Locate and identify every blood parasite.
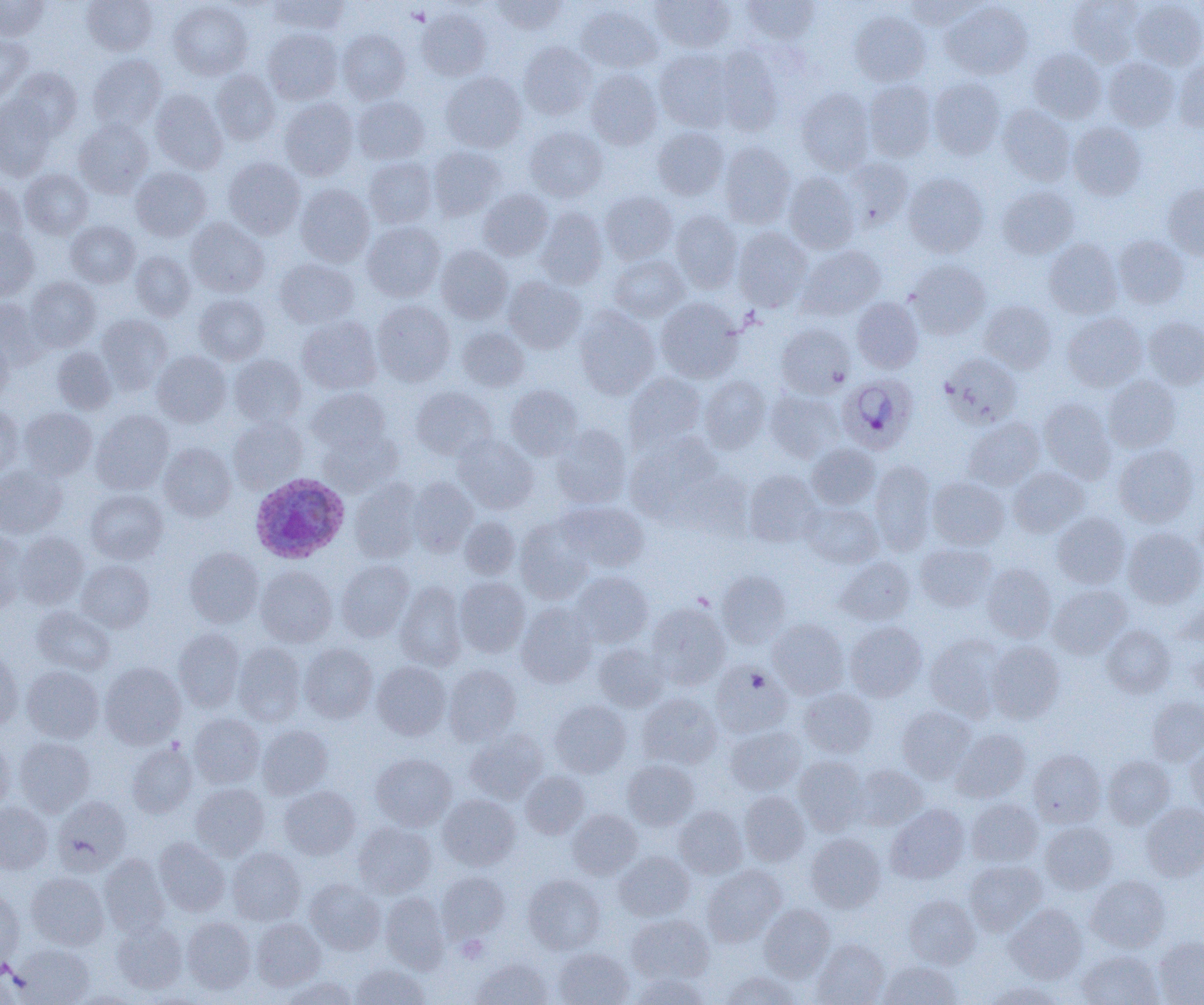

Approximate bounding boxes as [x1, y1, x2, y2] in pixels.
Plasmodium ovale-infected red blood cells: [837, 375, 918, 454], [249, 473, 350, 563].
No Plasmodium falciparum, Plasmodium malariae, Plasmodium vivax, Babesia divergens, or Trypanosoma brucei observed.

Summary:
  - Uninfected red blood cell locations: [82, 0, 157, 55], [268, 0, 350, 34], [489, 0, 567, 34], [651, 0, 736, 52], [740, 0, 820, 45], [903, 0, 982, 29], [1067, 0, 1143, 67], [0, 1, 49, 40], [168, 1, 252, 80], [942, 1, 1033, 79], [1130, 1, 1204, 70], [576, 4, 663, 73], [417, 7, 491, 81], [849, 10, 930, 86], [263, 28, 342, 104], [337, 29, 410, 103], [0, 34, 32, 102], [519, 42, 595, 120], [713, 45, 783, 135], [654, 49, 736, 132], [1028, 49, 1106, 122], [88, 54, 166, 132], [1103, 57, 1180, 131], [1174, 59, 1204, 132], [10, 68, 82, 138], [585, 68, 662, 150], [212, 70, 279, 145], [441, 72, 527, 152], [928, 77, 1005, 159], [864, 79, 937, 162], [150, 88, 227, 173], [796, 88, 875, 174], [0, 96, 56, 180], [352, 96, 430, 164], [280, 98, 358, 180], [998, 104, 1075, 185], [74, 119, 153, 198], [1069, 122, 1146, 200], [524, 126, 607, 202], [653, 127, 728, 200], [719, 142, 796, 228], [428, 146, 505, 220], [842, 156, 914, 231], [223, 157, 305, 239], [364, 157, 437, 228], [131, 166, 211, 241], [20, 169, 93, 238], [904, 172, 988, 257], [783, 173, 860, 253], [0, 181, 26, 249], [1163, 183, 1204, 260], [295, 184, 375, 266], [997, 186, 1079, 259], [478, 189, 553, 261], [600, 191, 677, 264], [535, 206, 608, 289], [670, 210, 743, 293], [186, 218, 269, 297], [66, 221, 139, 287], [363, 221, 445, 301], [733, 227, 812, 311], [0, 229, 38, 299], [1113, 234, 1190, 308], [1043, 239, 1122, 319], [436, 246, 513, 323], [798, 246, 886, 319], [130, 251, 196, 320], [608, 254, 689, 321], [275, 258, 358, 328], [907, 259, 991, 339], [25, 277, 101, 351], [503, 277, 586, 353], [194, 294, 270, 365], [851, 297, 923, 373], [655, 298, 744, 383], [0, 299, 46, 368], [372, 300, 455, 385], [980, 300, 1057, 372], [574, 307, 660, 399], [1062, 312, 1147, 391], [96, 314, 172, 393], [297, 315, 381, 394], [1142, 317, 1204, 389], [776, 323, 855, 398], [456, 327, 529, 392], [0, 336, 13, 403], [52, 347, 116, 415], [152, 350, 231, 427], [941, 353, 1022, 428], [229, 354, 306, 427], [625, 373, 707, 451], [700, 375, 772, 453], [1102, 376, 1181, 453], [506, 385, 584, 459], [411, 386, 496, 460], [307, 388, 389, 454], [765, 389, 845, 463], [1039, 398, 1117, 482], [0, 406, 23, 478], [19, 408, 97, 479], [92, 410, 174, 493], [229, 417, 307, 491], [963, 418, 1044, 490], [551, 425, 632, 508], [318, 429, 401, 496], [626, 433, 723, 520], [453, 434, 538, 514], [158, 443, 236, 521], [807, 443, 880, 510], [1113, 444, 1198, 526], [870, 460, 936, 554], [0, 464, 67, 538], [1008, 467, 1089, 537], [678, 469, 755, 540], [744, 469, 822, 547], [408, 477, 478, 556], [928, 477, 1009, 550], [348, 480, 423, 562], [86, 489, 168, 564], [559, 501, 650, 572], [801, 503, 883, 568], [1052, 512, 1130, 589], [460, 517, 520, 579], [515, 517, 594, 603], [1122, 527, 1204, 608], [0, 530, 27, 612], [14, 531, 89, 609], [915, 542, 997, 612], [184, 547, 264, 627], [836, 556, 916, 626], [77, 559, 154, 632], [336, 560, 414, 641], [982, 563, 1056, 642], [255, 566, 337, 647], [572, 571, 653, 648], [717, 571, 791, 648], [454, 577, 530, 657], [395, 581, 467, 670], [1048, 585, 1132, 658], [1175, 599, 1204, 646], [516, 602, 598, 687], [647, 602, 731, 689], [32, 606, 115, 675], [768, 618, 848, 699], [844, 621, 926, 702], [1102, 625, 1175, 697], [174, 629, 245, 711], [924, 634, 1006, 721], [987, 640, 1064, 723], [233, 643, 306, 725], [593, 643, 669, 711], [299, 644, 378, 722], [1187, 645, 1204, 701], [0, 650, 22, 731], [373, 661, 451, 741], [710, 661, 793, 739], [100, 662, 185, 748], [443, 665, 521, 744], [22, 666, 103, 743], [798, 688, 878, 757], [637, 692, 722, 769], [1147, 697, 1204, 765], [549, 699, 631, 777], [897, 705, 976, 783], [189, 713, 264, 788], [257, 725, 333, 799], [726, 726, 806, 795], [465, 729, 547, 804], [951, 729, 1031, 803], [14, 737, 95, 815], [0, 739, 14, 812], [126, 742, 197, 817], [1185, 742, 1204, 814], [1028, 749, 1106, 827], [371, 753, 456, 830], [793, 755, 869, 835], [1102, 755, 1175, 829], [622, 759, 699, 830], [852, 764, 927, 830], [520, 770, 590, 838], [190, 783, 269, 860], [279, 785, 360, 859], [739, 790, 810, 866], [438, 794, 519, 870], [52, 796, 131, 874], [966, 798, 1042, 867], [0, 802, 52, 873], [886, 803, 969, 884], [1141, 803, 1204, 881], [674, 806, 747, 878], [568, 809, 642, 879], [354, 822, 436, 898], [1040, 822, 1117, 893], [806, 833, 885, 912], [154, 837, 230, 917], [227, 847, 306, 925], [615, 851, 694, 920], [99, 854, 169, 937], [964, 859, 1046, 935], [702, 865, 786, 946], [27, 872, 109, 950], [436, 872, 510, 944], [523, 874, 605, 954], [1086, 875, 1170, 952], [305, 879, 386, 955], [0, 888, 23, 969], [381, 892, 450, 972], [904, 895, 980, 968], [759, 904, 835, 981], [1006, 904, 1087, 984], [627, 914, 713, 983], [182, 917, 256, 993], [251, 918, 325, 990], [111, 921, 187, 994], [1153, 936, 1204, 1005], [813, 938, 889, 1005], [12, 944, 94, 1004], [553, 948, 633, 1005], [1077, 950, 1162, 1005], [472, 957, 552, 1005], [879, 960, 961, 1004], [350, 963, 429, 1004], [719, 970, 802, 1004], [629, 972, 709, 1004], [281, 976, 358, 1005], [982, 981, 1067, 1005], [66, 989, 139, 1004]
  - Slide-level diagnosis: Plasmodium ovale
  - Magnification: 1000x
  - Modality: optical microscopy
  - Field of view: one of a larger specimen
  - Preparation: thin blood smear
  - Image size: 1204×1005 pixels